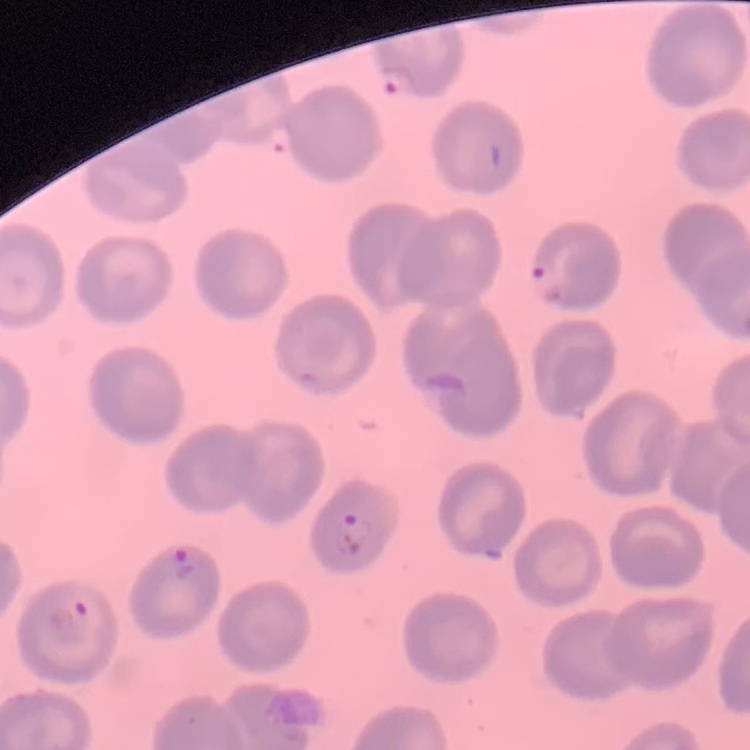
The red blood cells show no rouleaux formation. Stained with either Field's or Giemsa. Thin blood film. One tile cut from a larger photomicrograph.